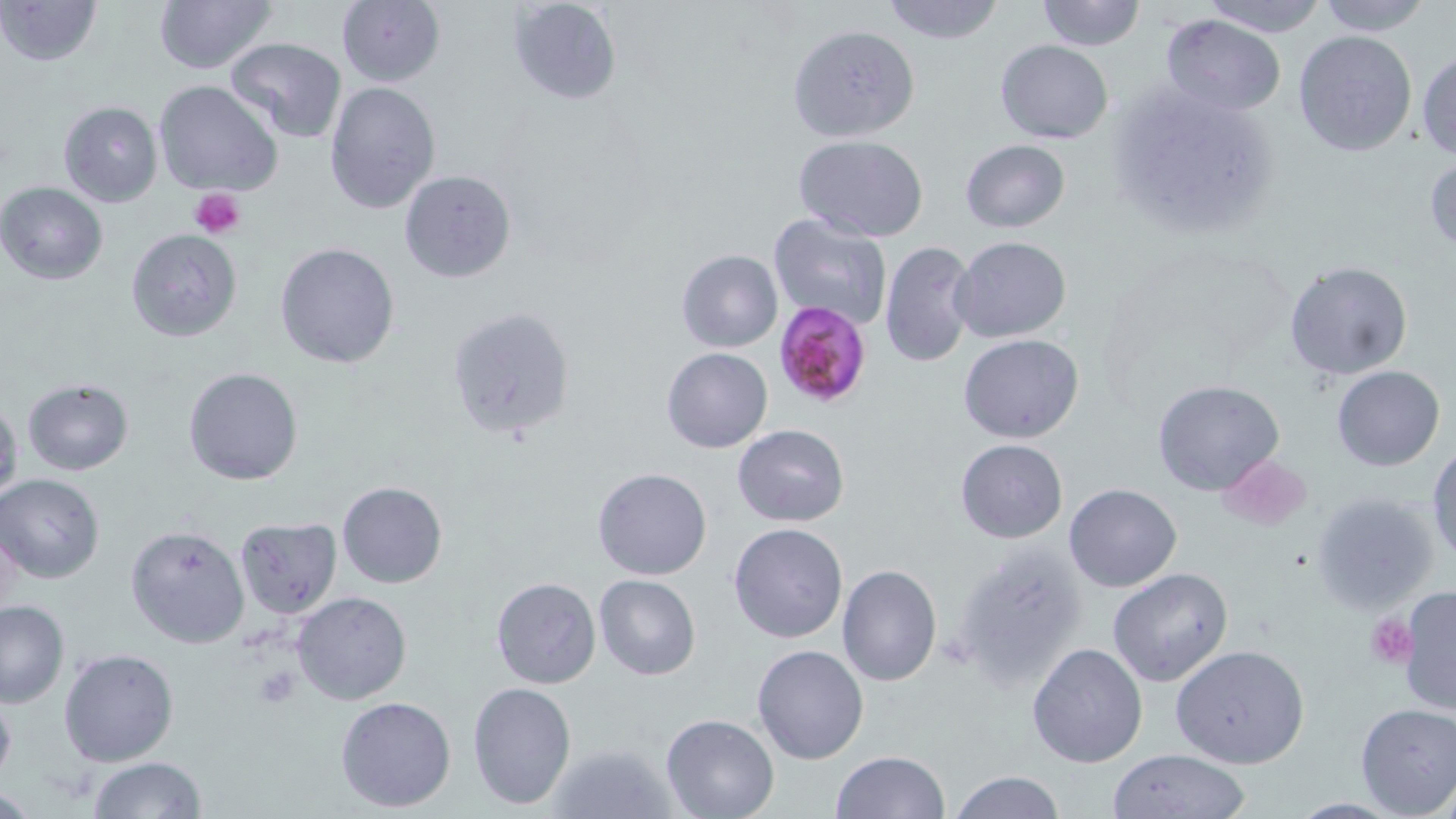
Approximate bounding boxes as named x1/y1/x2/y2 corners in pixels. Plasmodium falciparum-infected red blood cell locations: (x1=773, y1=301, x2=873, y2=410). Uninfected red blood cell locations: (x1=0, y1=0, x2=102, y2=67), (x1=154, y1=0, x2=279, y2=74), (x1=507, y1=0, x2=624, y2=107), (x1=879, y1=0, x2=1007, y2=44), (x1=1038, y1=0, x2=1144, y2=50), (x1=1199, y1=0, x2=1327, y2=36), (x1=1314, y1=0, x2=1435, y2=36), (x1=336, y1=1, x2=445, y2=87), (x1=1160, y1=13, x2=1285, y2=115), (x1=791, y1=25, x2=920, y2=141), (x1=1293, y1=30, x2=1418, y2=157), (x1=223, y1=38, x2=348, y2=143), (x1=994, y1=40, x2=1113, y2=143), (x1=1415, y1=49, x2=1456, y2=160), (x1=153, y1=79, x2=283, y2=197), (x1=325, y1=81, x2=442, y2=215), (x1=1107, y1=81, x2=1284, y2=240), (x1=56, y1=100, x2=164, y2=207), (x1=794, y1=134, x2=929, y2=240), (x1=960, y1=139, x2=1070, y2=233), (x1=1424, y1=152, x2=1456, y2=256), (x1=398, y1=170, x2=516, y2=283), (x1=0, y1=182, x2=108, y2=285), (x1=769, y1=214, x2=893, y2=329), (x1=125, y1=229, x2=242, y2=343), (x1=950, y1=235, x2=1071, y2=343), (x1=880, y1=240, x2=977, y2=368), (x1=275, y1=243, x2=401, y2=369), (x1=676, y1=249, x2=783, y2=353), (x1=1285, y1=260, x2=1412, y2=380), (x1=445, y1=306, x2=575, y2=442), (x1=957, y1=333, x2=1085, y2=443), (x1=660, y1=347, x2=772, y2=453), (x1=1331, y1=365, x2=1445, y2=472), (x1=184, y1=366, x2=304, y2=486), (x1=23, y1=377, x2=133, y2=475), (x1=1153, y1=381, x2=1285, y2=497), (x1=0, y1=393, x2=23, y2=513), (x1=734, y1=423, x2=849, y2=527), (x1=955, y1=438, x2=1068, y2=542), (x1=1427, y1=443, x2=1456, y2=564), (x1=592, y1=466, x2=712, y2=580), (x1=1, y1=473, x2=106, y2=583), (x1=337, y1=481, x2=447, y2=588), (x1=1064, y1=484, x2=1182, y2=592), (x1=1310, y1=490, x2=1443, y2=614), (x1=234, y1=517, x2=343, y2=620), (x1=1, y1=519, x2=23, y2=624), (x1=728, y1=522, x2=849, y2=643), (x1=125, y1=524, x2=250, y2=648), (x1=953, y1=541, x2=1091, y2=691), (x1=836, y1=565, x2=941, y2=686), (x1=1106, y1=567, x2=1234, y2=687), (x1=593, y1=574, x2=701, y2=680), (x1=490, y1=576, x2=601, y2=689), (x1=1397, y1=586, x2=1455, y2=716), (x1=292, y1=591, x2=412, y2=705), (x1=1, y1=598, x2=68, y2=707), (x1=1026, y1=643, x2=1148, y2=768), (x1=1172, y1=644, x2=1310, y2=769), (x1=752, y1=645, x2=869, y2=765), (x1=59, y1=647, x2=179, y2=767), (x1=467, y1=681, x2=576, y2=808), (x1=0, y1=688, x2=16, y2=787), (x1=335, y1=696, x2=457, y2=811), (x1=1354, y1=702, x2=1456, y2=817), (x1=661, y1=714, x2=779, y2=819), (x1=543, y1=742, x2=679, y2=819), (x1=1105, y1=748, x2=1253, y2=819), (x1=830, y1=750, x2=949, y2=819), (x1=86, y1=757, x2=207, y2=818), (x1=948, y1=772, x2=1066, y2=818). Platelet locations: (x1=190, y1=187, x2=246, y2=240), (x1=1216, y1=452, x2=1313, y2=532), (x1=1363, y1=609, x2=1416, y2=667), (x1=249, y1=667, x2=304, y2=707). Slide-level diagnosis: Plasmodium falciparum. Light microscopy. Single field of view. 1000x magnification. Image is 1456×819 pixels. Thin blood film. May-Grünwald-Giemsa-stained preparation.